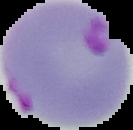

{
  "image_type": "cell region segmented out of the field of view; surrounding area masked to black",
  "image_size": "133×130 pixels",
  "preparation": "thin blood smear",
  "malaria_status": "parasitized"
}